Name the parasite shown.
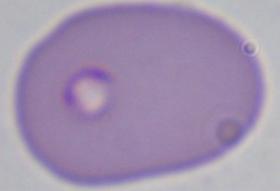
This is Babesia.

magnification: 1000x
modality: photomicrograph